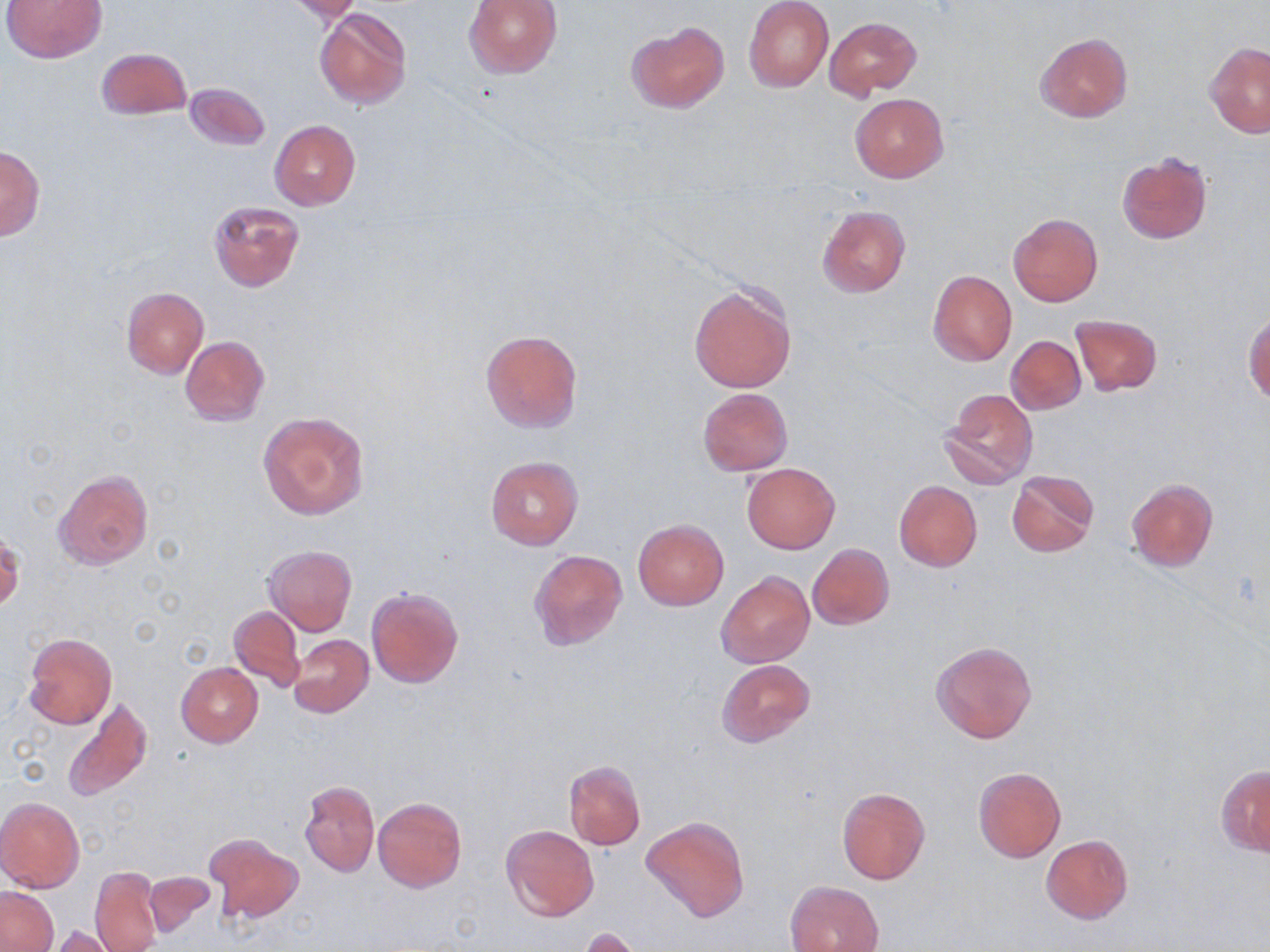
slide_level_diagnosis: no evidence of blood parasites
magnification: 1000x
stain: May-Grünwald-Giemsa
field_of_view: single
uninfected_red_blood_cell_locations: 'approximate bounding boxes as (x1,y1)-(x2,y2) corner pairs in pixels: (3,0)-(106,63), (464,0)-(561,78), (744,0)-(834,92), (282,1)-(366,23), (314,8)-(411,109), (824,17)-(920,98), (626,20)-(728,112), (1035,31)-(1132,122), (1206,43)-(1270,137), (96,47)-(192,120), (185,82)-(270,150), (849,92)-(948,183), (269,119)-(361,210), (0,147)-(45,241), (1116,152)-(1213,245), (209,199)-(304,292), (817,205)-(910,297), (1007,211)-(1103,306), (928,270)-(1017,367), (689,282)-(796,393), (121,286)-(208,378), (1243,310)-(1270,402), (1070,313)-(1163,396), (480,329)-(583,434), (181,336)-(269,427), (1006,336)-(1086,415), (696,388)-(794,476), (942,389)-(1038,489), (258,411)-(370,521), (485,456)-(583,550), (741,462)-(840,554), (54,468)-(153,570), (1007,470)-(1099,557), (1126,478)-(1218,572), (894,480)-(982,571), (632,519)-(729,611), (0,531)-(24,612), (808,544)-(894,629), (264,545)-(358,636), (529,550)-(627,651), (716,571)-(814,668), (367,586)-(463,687), (230,606)-(305,689), (22,632)-(117,729), (288,634)-(373,717), (930,641)-(1037,744), (716,658)-(815,748), (176,662)-(262,747), (61,697)-(151,803), (563,760)-(646,850), (1217,764)-(1270,856), (973,767)-(1065,861), (300,781)-(378,878), (836,785)-(931,885), (0,796)-(84,893), (372,797)-(466,892), (641,815)-(750,922), (500,824)-(599,922), (206,834)-(303,924), (1041,834)-(1133,923), (90,866)-(162,952), (143,872)-(215,938), (785,880)-(883,952), (0,887)-(57,951), (48,926)-(122,951), (579,928)-(646,952)'
preparation: thin blood smear
image_size: 1270×952 pixels
modality: light microscopy